Describe the morphology of the red blood cells.
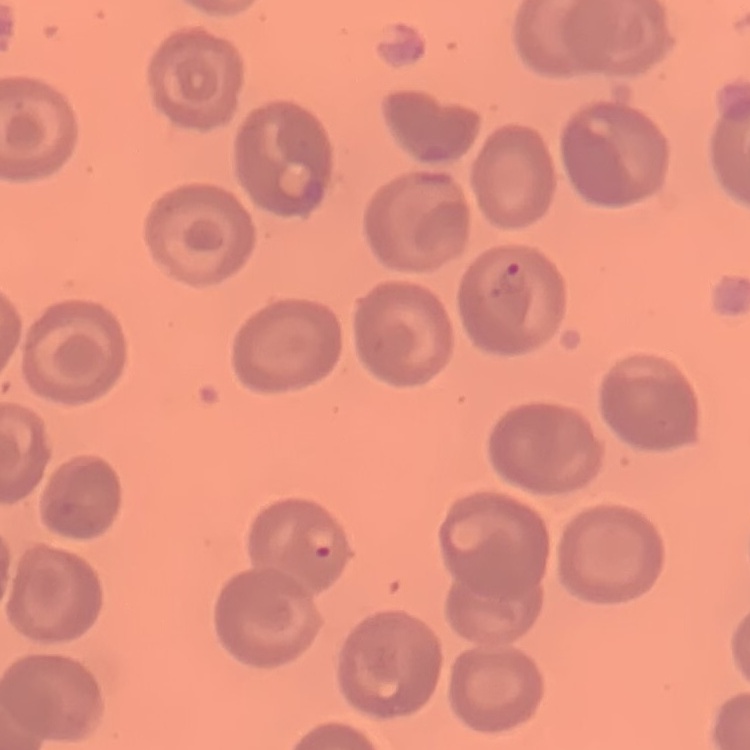

They show no rouleaux formation.

Thin peripheral smear. One tile cut from a larger photomicrograph. Stained with either Field's or Giemsa.